Identify the blood parasite species.
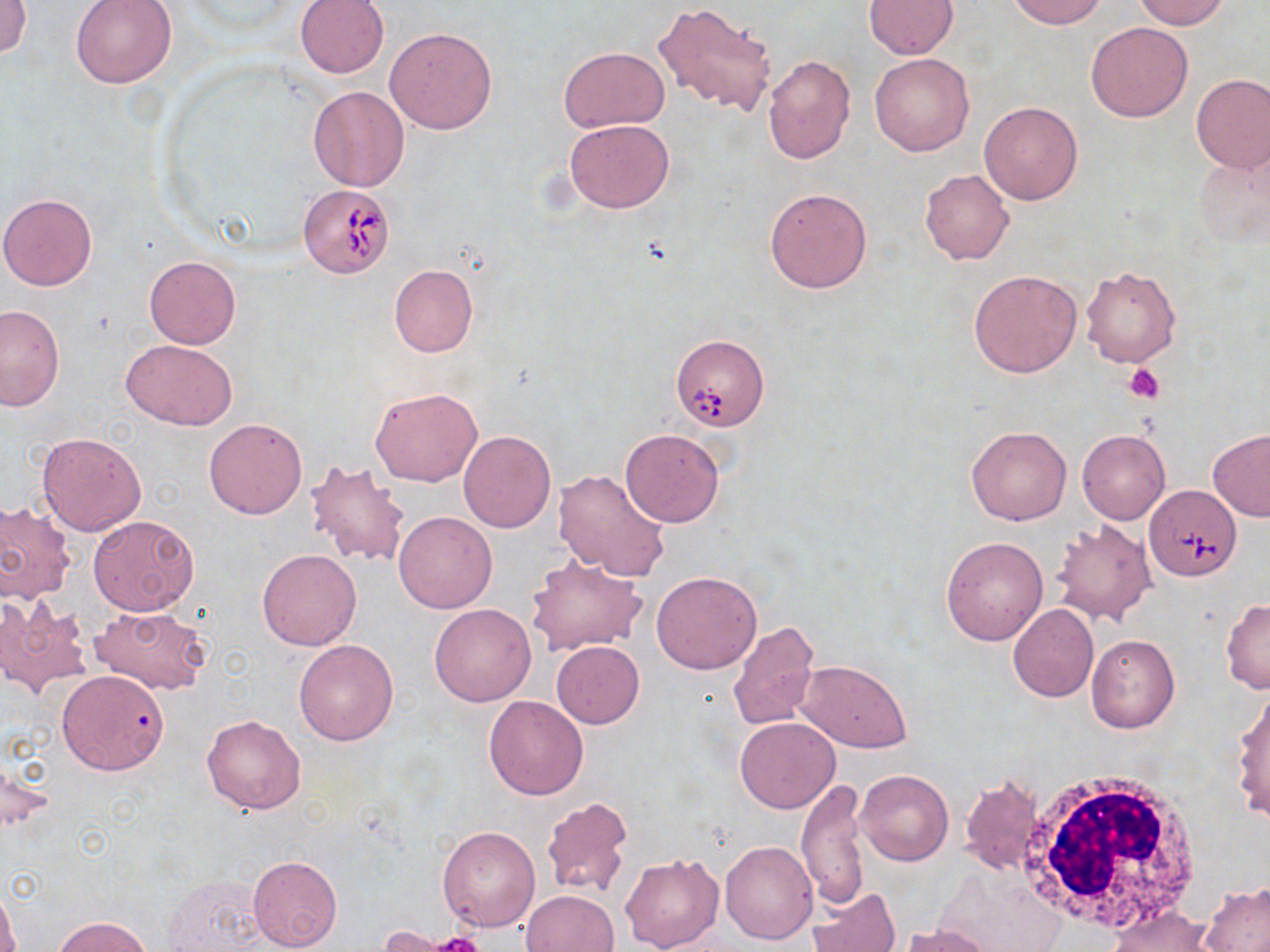
Babesia divergens.

Approximate bounding boxes as (x1, y1, x2, y2) in pixels. White blood cell locations: (1018, 768, 1204, 933). Uninfected red blood cell locations: (70, 0, 177, 88), (295, 0, 389, 79), (1006, 0, 1107, 28), (1133, 0, 1228, 29), (0, 1, 32, 60), (864, 1, 956, 58), (653, 2, 778, 118), (1085, 22, 1193, 122), (384, 28, 497, 135), (559, 47, 667, 133), (870, 53, 974, 156), (762, 55, 856, 165), (1191, 75, 1270, 173), (308, 86, 409, 191), (980, 102, 1082, 205), (565, 119, 674, 213), (1192, 150, 1269, 250), (919, 169, 1015, 265), (765, 187, 873, 293), (0, 193, 97, 291), (145, 256, 240, 349), (389, 265, 478, 358), (1080, 265, 1181, 368), (968, 269, 1083, 378), (1, 304, 66, 412), (122, 338, 237, 430), (371, 387, 481, 487), (203, 419, 307, 519), (966, 425, 1071, 525), (620, 429, 726, 528), (1207, 429, 1270, 522), (458, 430, 555, 532), (1076, 430, 1170, 525), (35, 431, 147, 537), (306, 458, 412, 568), (553, 469, 671, 583), (0, 499, 74, 604), (394, 511, 496, 613), (90, 516, 198, 615), (1050, 519, 1157, 625), (940, 536, 1048, 644), (258, 549, 361, 651), (527, 555, 647, 656), (650, 570, 763, 674), (0, 597, 90, 699), (1221, 598, 1270, 693), (429, 603, 536, 706), (90, 604, 210, 694), (1008, 604, 1099, 702), (727, 620, 821, 731), (1086, 633, 1180, 733), (293, 639, 398, 746), (552, 641, 644, 728), (796, 659, 913, 752), (56, 669, 170, 775), (1230, 687, 1270, 823), (483, 695, 589, 800), (201, 714, 306, 814), (736, 717, 840, 813), (854, 770, 953, 866), (960, 776, 1044, 873), (797, 779, 868, 911), (540, 796, 633, 900), (437, 825, 540, 932), (720, 840, 818, 945), (620, 852, 724, 952), (248, 855, 343, 952), (935, 867, 1062, 951), (161, 874, 269, 951), (1200, 883, 1270, 951), (0, 886, 18, 952), (805, 887, 900, 952), (522, 888, 619, 952), (1106, 906, 1214, 952), (52, 915, 154, 952), (898, 925, 997, 952), (376, 926, 456, 951). Babesia divergens-infected red blood cell locations: (297, 187, 395, 278), (671, 334, 770, 432), (1146, 483, 1240, 580). Platelet locations: (1125, 364, 1165, 404), (432, 933, 484, 952). 1000x magnification. May-Grünwald-Giemsa stain. Optical microscopy. Image is 1270×952 pixels. Thin blood film. One field of a larger specimen.